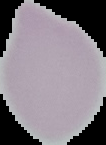

{
  "image_type": "cell region segmented out of the field of view; surrounding area masked to black",
  "result": "no malaria parasites seen",
  "preparation": "thin blood film",
  "image_size": "106×145 pixels"
}